Describe the morphology of the red blood cells.
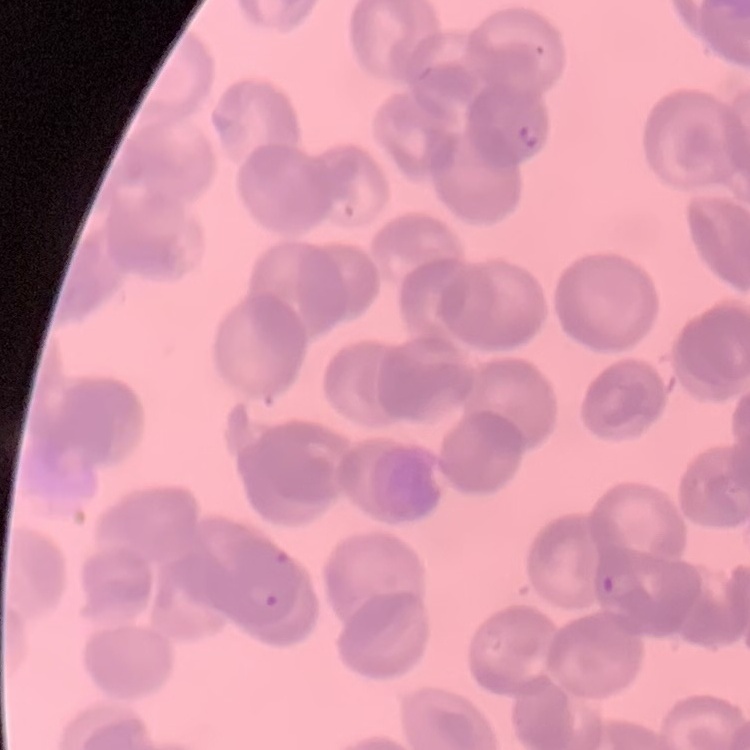
Rouleaux formation.

stain = Field's or Giemsa
image type = square crop of a larger photomicrograph
preparation = thin blood film